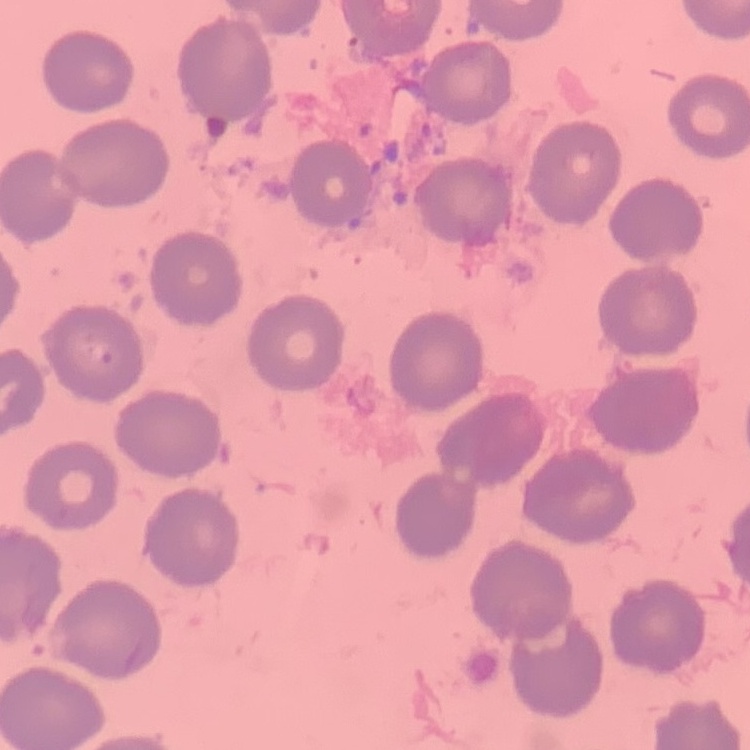

Summary:
  - Red blood cell morphology: no rouleaux formation
  - Stain: Field's or Giemsa
  - Preparation: thin blood smear
  - Image type: square crop of a larger photomicrograph